Name the parasite shown.
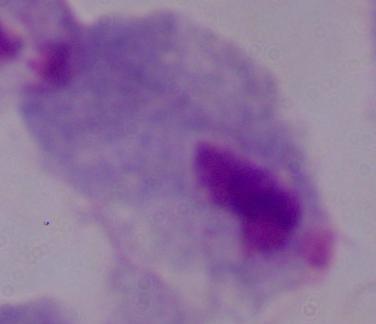

A trichomonad.

{
  "modality": "photomicrograph",
  "magnification": "1000x"
}